Identify the parasite.
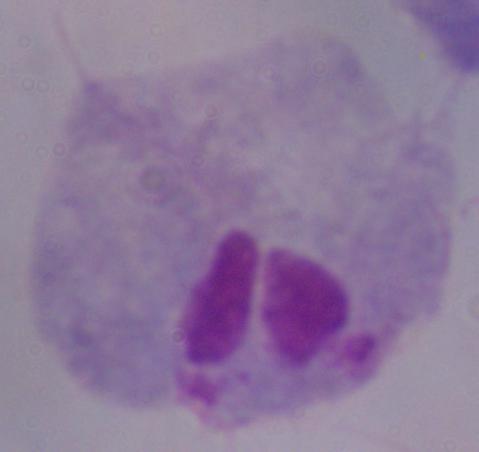
This is a trichomonad.

modality = micrograph
magnification = 1000x